Locate and identify every blood parasite.
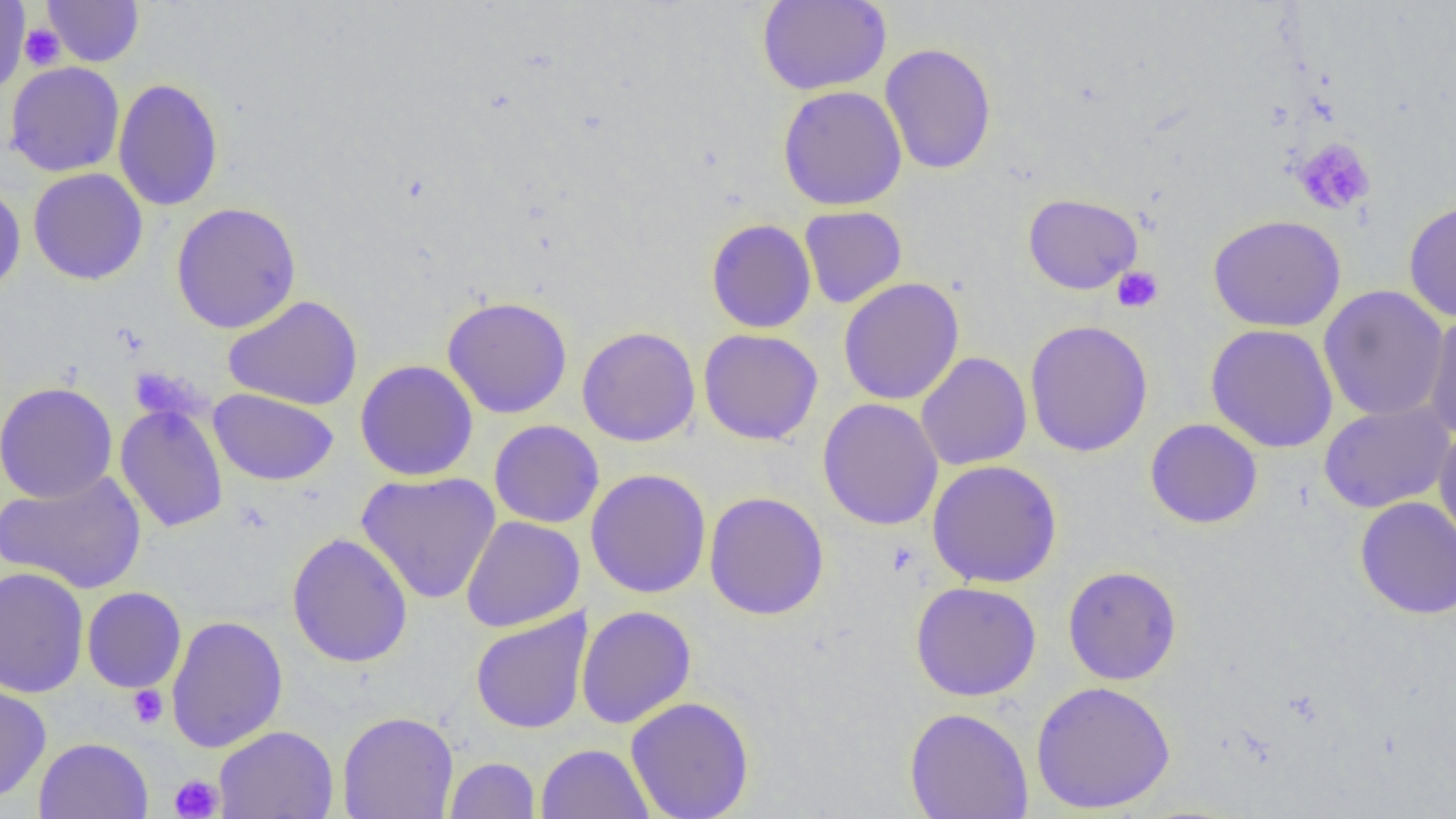

No blood parasites observed.

Approximate bounding boxes as [x1, y1, x2, y2] in pixels. Platelet locations: [20, 23, 66, 70], [1292, 137, 1376, 216], [1112, 266, 1164, 313], [127, 685, 169, 729], [170, 774, 224, 818]. Uninfected red blood cell locations: [0, 0, 30, 95], [42, 0, 144, 67], [756, 0, 891, 95], [880, 43, 997, 175], [5, 61, 125, 177], [113, 77, 224, 212], [777, 84, 907, 211], [28, 168, 148, 285], [0, 183, 26, 297], [1022, 193, 1143, 294], [1403, 199, 1456, 322], [171, 202, 302, 333], [799, 205, 907, 309], [1207, 214, 1346, 332], [706, 218, 817, 334], [838, 277, 965, 405], [1318, 285, 1450, 422], [223, 295, 363, 410], [442, 295, 573, 418], [1422, 311, 1455, 441], [1024, 319, 1154, 457], [1205, 323, 1339, 453], [576, 326, 701, 447], [697, 329, 823, 445], [915, 351, 1032, 471], [355, 359, 478, 481], [0, 382, 117, 504], [209, 388, 338, 485], [817, 398, 944, 531], [115, 401, 229, 533], [1319, 401, 1455, 513], [1145, 418, 1263, 529], [489, 420, 604, 528], [1433, 426, 1456, 546], [927, 460, 1063, 588], [586, 469, 712, 598], [0, 470, 147, 594], [356, 471, 501, 604], [703, 491, 829, 620], [1355, 496, 1456, 619], [461, 515, 585, 632], [286, 532, 413, 668], [1063, 565, 1182, 685], [0, 566, 89, 698], [910, 581, 1042, 701], [82, 587, 186, 692], [576, 605, 696, 729], [470, 609, 592, 735], [166, 615, 288, 754], [0, 678, 51, 802], [1031, 680, 1175, 814], [625, 696, 755, 819], [904, 707, 1034, 819], [337, 710, 458, 819], [213, 725, 339, 819], [34, 737, 153, 819], [535, 743, 653, 819], [444, 757, 540, 818]. Slide-level diagnosis: negative for blood parasites. Single field of view. Thin blood smear. Image is 1456×819 pixels. 1000x magnification. Light microscopy.